Name the cell type shown.
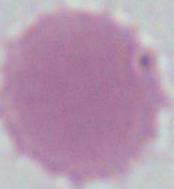
An erythrocyte.

Micrograph. Captured at 1000x magnification.